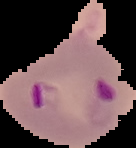
preparation = thin blood film
malaria status = parasitized
image type = segmented cell region with the area outside set to black
image size = 136×148 pixels